Point out each leukocyte.
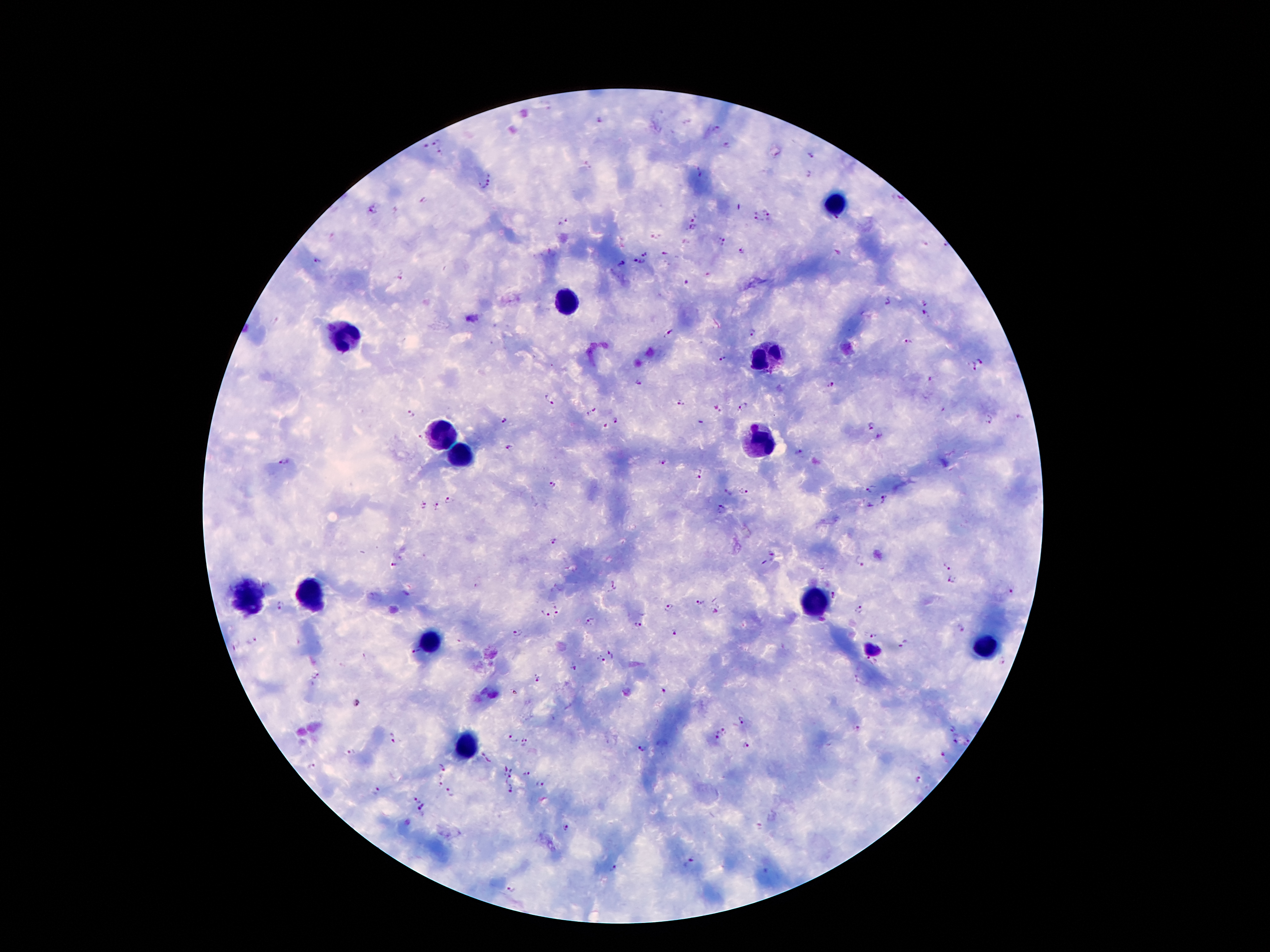
Approximate centers as [x, y] in pixels.
Leukocytes: [835, 200], [568, 299], [341, 337], [765, 360], [442, 433], [759, 440], [452, 454], [310, 591], [244, 595], [816, 605], [431, 641], [988, 645], [465, 746].

Plasmodium parasite locations: [601, 121], [688, 122], [718, 130], [436, 142], [426, 144], [728, 144], [441, 154], [811, 155], [589, 165], [701, 173], [809, 176], [491, 177], [484, 186], [423, 199], [900, 199], [374, 210], [769, 210], [694, 217], [568, 219], [757, 220], [836, 220], [560, 224], [692, 228], [721, 242], [926, 242], [947, 244], [742, 252], [646, 253], [666, 253], [839, 253], [318, 260], [639, 261], [622, 264], [400, 275], [709, 275], [687, 282], [888, 300], [927, 301], [927, 315], [473, 319], [751, 331], [669, 332], [908, 343], [981, 360], [723, 361], [973, 366], [639, 384], [831, 385], [548, 396], [679, 404], [744, 406], [717, 408], [590, 411], [411, 414], [1020, 417], [988, 419], [617, 420], [503, 422], [699, 424], [870, 425], [605, 426], [417, 437], [879, 438], [509, 447], [798, 451], [284, 460], [664, 463], [699, 475], [552, 484], [870, 489], [745, 493], [728, 494], [885, 497], [448, 500], [870, 505], [421, 506], [436, 508], [721, 509], [551, 540], [772, 552], [861, 561], [949, 564], [394, 565], [952, 580], [613, 584], [1010, 592], [835, 596], [701, 603], [278, 606], [670, 606], [861, 609], [557, 610], [543, 614], [589, 621], [637, 623], [961, 627], [675, 631], [518, 632], [871, 632], [253, 641], [905, 644], [237, 645], [415, 650], [612, 652], [601, 660], [871, 661], [1002, 661], [573, 667], [316, 675], [536, 678], [857, 681], [664, 691], [356, 704], [743, 717], [955, 726], [857, 729], [724, 730], [391, 737], [512, 737], [716, 737], [955, 742], [968, 742], [526, 744], [746, 746], [641, 748], [350, 752], [942, 754], [485, 758], [443, 765], [312, 766], [509, 766], [527, 772], [508, 779], [917, 780], [439, 784], [538, 785], [377, 791], [511, 792], [451, 794], [415, 800], [421, 808], [565, 827], [758, 827], [688, 862], [613, 870]. Image is 1270×952 pixels. Smartphone photograph taken through the microscope eyepiece. Patient malaria status: positive for Plasmodium falciparum. Giemsa-stained preparation. Thick blood film. 100x magnification. One field from this slide.